Assess the morphology of the red blood cells.
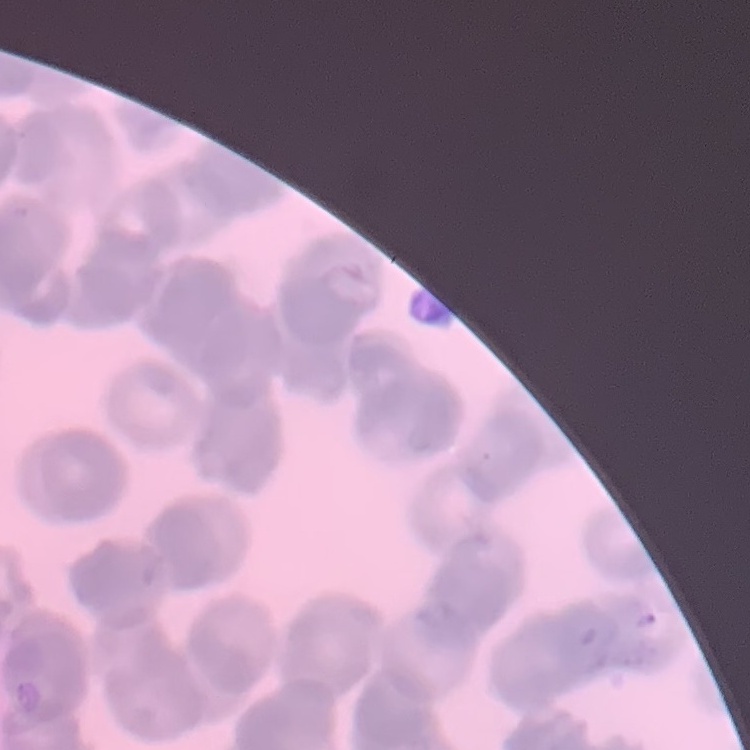
Rouleaux formation.

image type = square crop of a larger photomicrograph
stain = Field's or Giemsa
preparation = thin peripheral smear